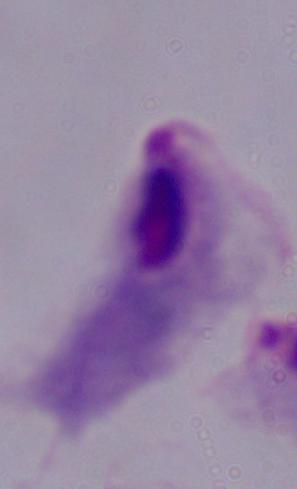

{
  "magnification": "1000x",
  "identification": "trichomonad",
  "modality": "micrograph"
}